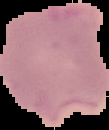
image type = cell region segmented out of the field of view; surrounding area masked to black
image size = 109×130 pixels
preparation = thin blood film
result = malaria parasites identified